Comment on the morphology of the erythrocytes.
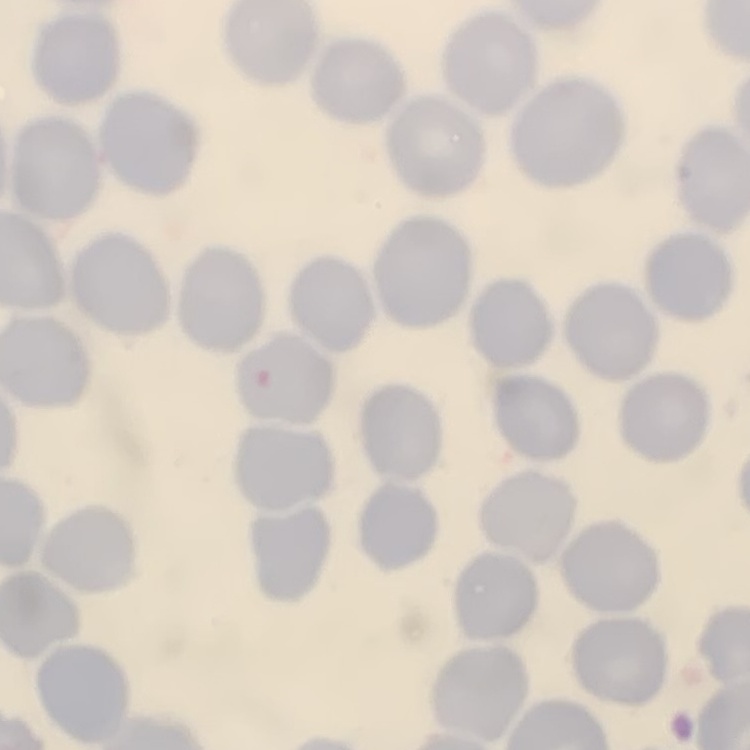

They show no rouleaux formation.

Thin peripheral smear. Square crop of a larger photomicrograph. Field's or Giemsa stain.